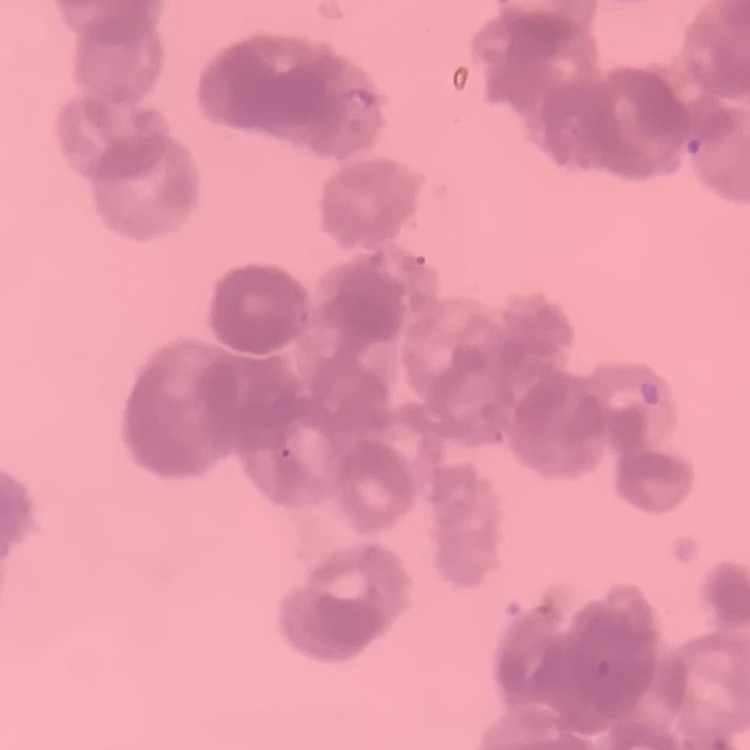

The red blood cells exhibit rouleaux formation. Thin peripheral smear. Stained with either Field's or Giemsa. One tile cut from a larger photomicrograph.